Report the malaria status of this cell.
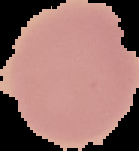
Uninfected.

preparation = thin blood film
image size = 139×151 pixels
image type = segmented cell region on a black background